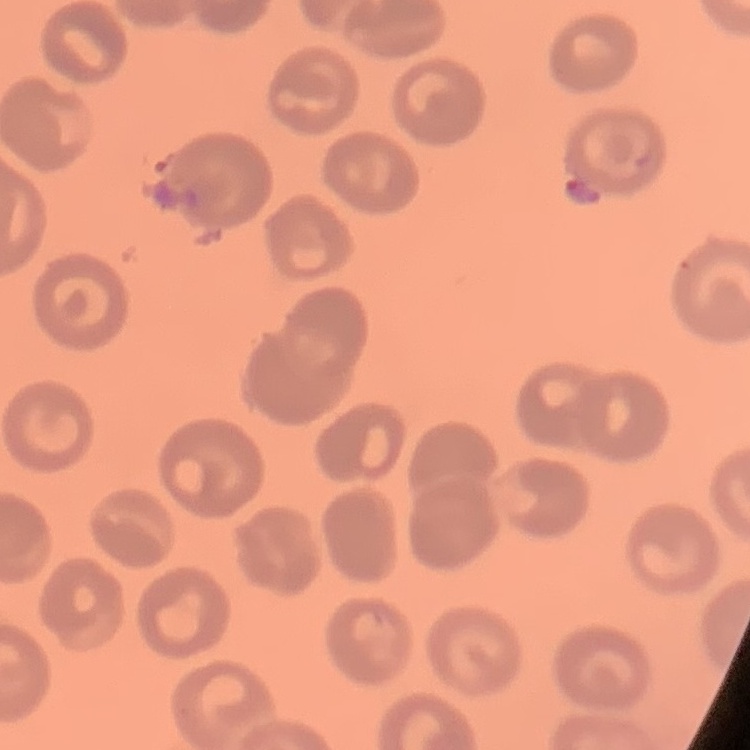

{
  "erythrocyte_morphology": "no rouleaux formation",
  "preparation": "thin blood film",
  "image_type": "one tile cut from a larger photomicrograph",
  "stain": "Field's or Giemsa"
}